Assess this cell for malaria.
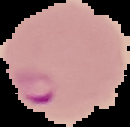
It is parasitized.

Summary:
  - Preparation: thin blood film
  - Image type: cell region segmented out of the field of view; surrounding area masked to black
  - Image size: 130×127 pixels